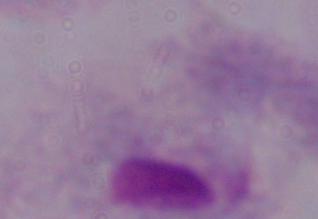
Summary:
  - Identification: trichomonad
  - Magnification: 1000x
  - Modality: photomicrograph